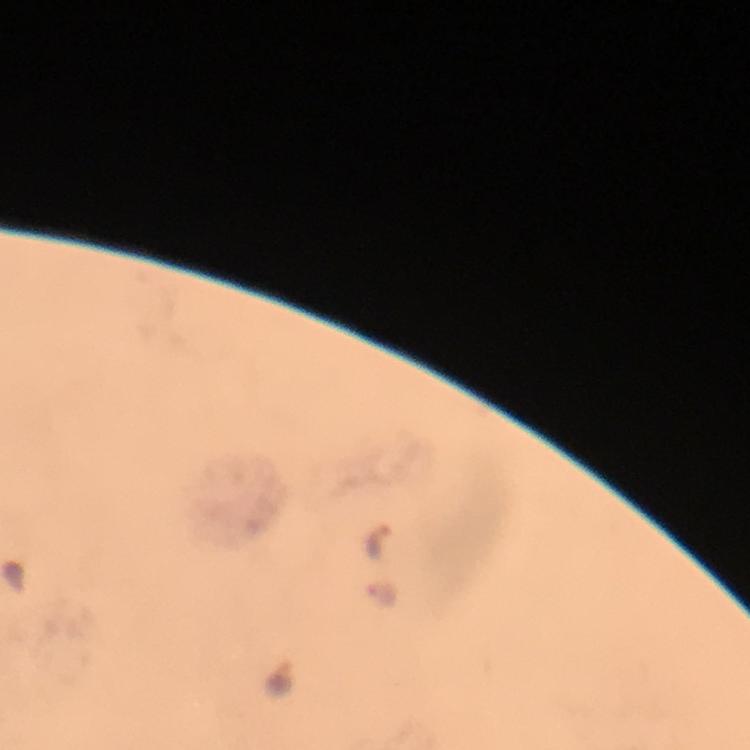
Approximate centers as [x, y] in pixels. Malaria parasite locations: [378, 543], [382, 594]. Image is 750×750 pixels. Smartphone photograph taken through a microscope. Thick blood smear. Giemsa-stained preparation. 100x magnification. Immersion oil was used. A crop from one field of view. From a diagnostic examination for malaria.